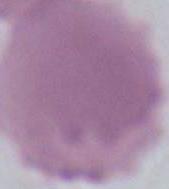

Summary:
  - Modality: micrograph
  - Magnification: 1000x
  - Identification: erythrocyte